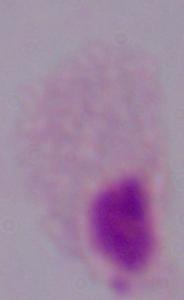

modality: micrograph
identification: trichomonad
magnification: 1000x